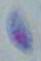

Summary:
  - Magnification: 1000x
  - Identification: Toxoplasma gondii
  - Modality: micrograph